Give the position of every leukocyte visible.
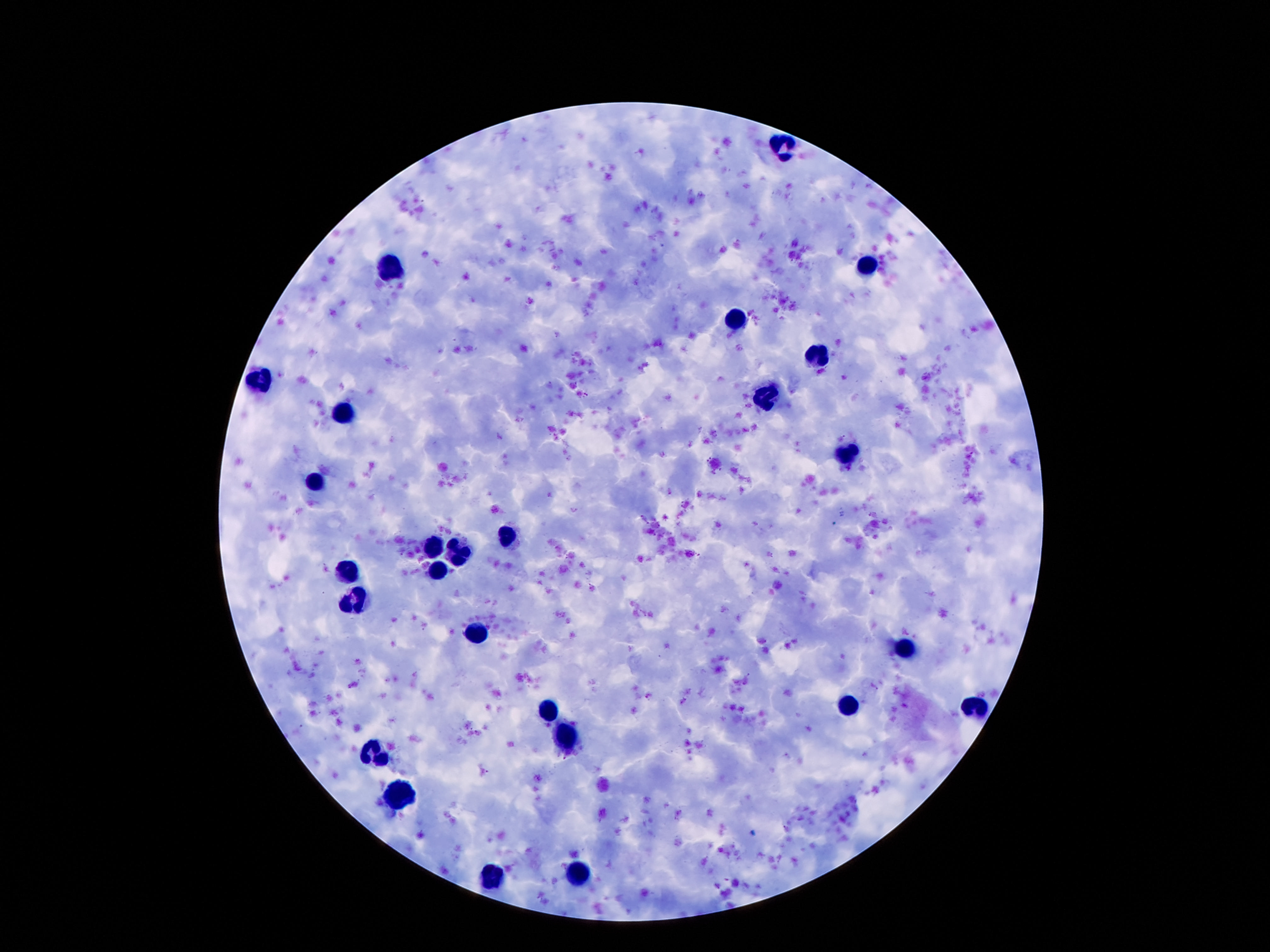

Approximate centers as {x, y} in pixels.
Leukocytes: {782, 145}, {390, 264}, {868, 267}, {732, 322}, {816, 360}, {263, 379}, {766, 401}, {342, 414}, {848, 453}, {314, 485}, {508, 536}, {431, 550}, {457, 553}, {349, 572}, {437, 572}, {357, 600}, {478, 636}, {906, 649}, {846, 705}, {975, 705}, {551, 710}, {564, 738}, {377, 750}, {400, 796}, {577, 874}, {495, 875}.

Patient malaria status: negative. Image is 1270×952 pixels. One field from this slide. Smartphone photograph taken through the microscope eyepiece. Thick blood smear. 100x magnification. Giemsa stain.